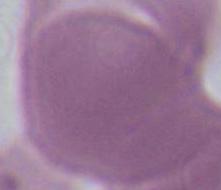
magnification = 1000x
identification = red blood cell
modality = photomicrograph